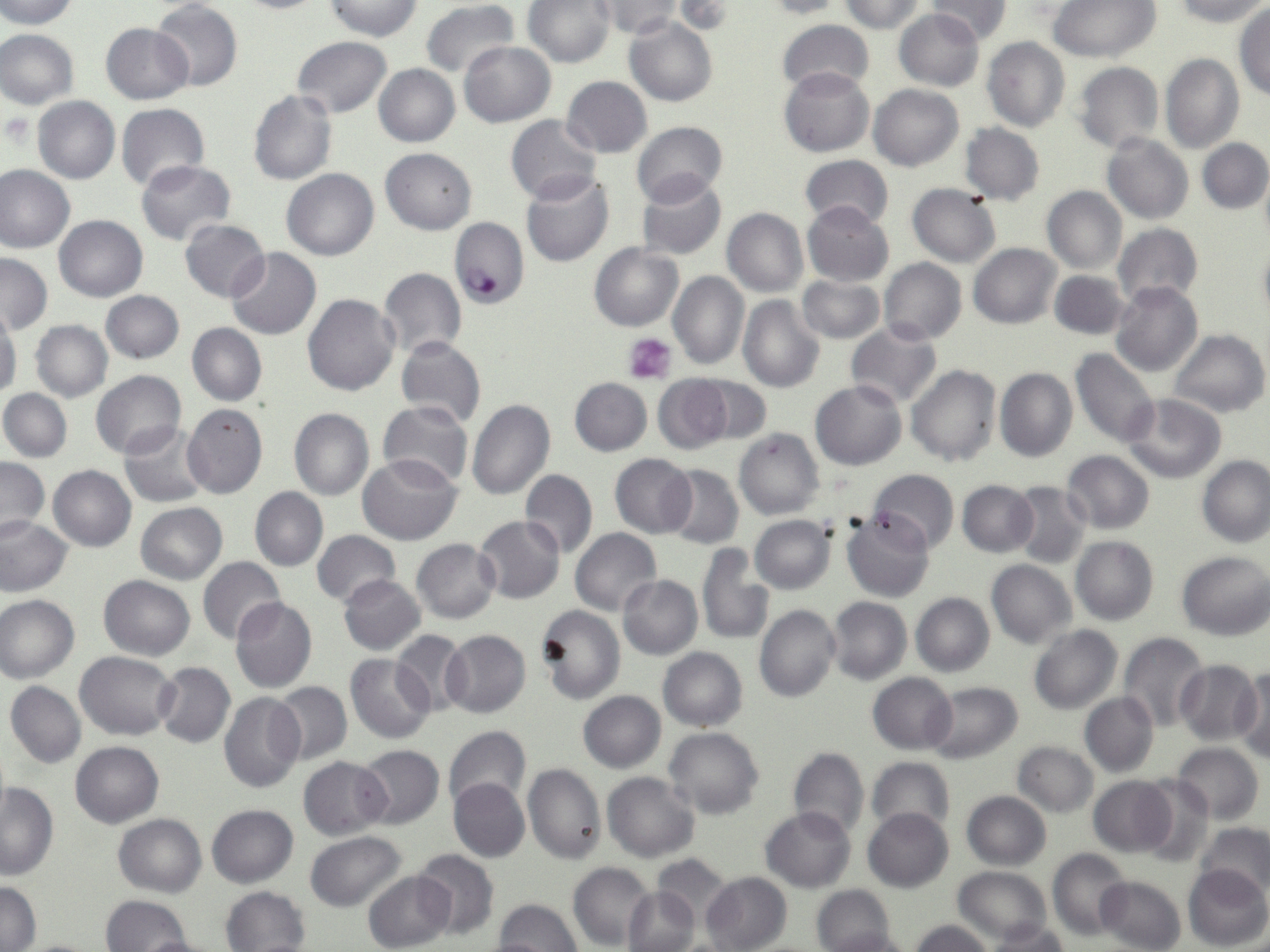

Summary:
  - Coordinate format: approximate bounding boxes as (x1,y1)-(x2,y2) corner pairs in pixels
  - Plasmodium falciparum-infected red blood cell locations: (449,217)-(528,309)
  - Uninfected red blood cell locations: (0,0)-(78,29), (227,0)-(332,13), (320,0)-(422,40), (421,0)-(520,80), (758,0)-(843,19), (836,0)-(929,32), (924,0)-(1010,43), (1049,0)-(1158,61), (1169,0)-(1270,26), (150,1)-(242,92), (523,1)-(615,69), (595,1)-(681,38), (675,1)-(736,35), (1233,4)-(1270,100), (894,8)-(984,91), (625,15)-(718,106), (777,20)-(874,98), (101,23)-(192,103), (0,28)-(79,108), (292,36)-(392,118), (982,38)-(1070,132), (458,41)-(556,126), (1160,53)-(1243,154), (1073,62)-(1164,154), (374,64)-(459,147), (779,67)-(874,157), (562,76)-(652,157), (869,84)-(964,170), (248,90)-(336,185), (33,96)-(121,184), (117,103)-(209,193), (505,114)-(603,203), (631,120)-(728,205), (960,123)-(1045,204), (1103,134)-(1193,224), (1198,139)-(1270,213), (380,147)-(476,234), (799,154)-(894,229), (136,159)-(237,245), (1258,164)-(1270,252), (0,165)-(75,254), (282,168)-(379,261), (521,173)-(613,267), (637,175)-(727,260), (906,183)-(1001,267), (1041,185)-(1127,274), (802,201)-(894,286), (722,207)-(808,295), (54,215)-(147,302), (180,219)-(270,302), (1112,223)-(1203,307), (1256,242)-(1270,324), (588,243)-(683,331), (969,243)-(1061,327), (225,248)-(322,339), (0,253)-(52,335), (879,258)-(966,344), (378,268)-(466,359), (1051,270)-(1129,340), (669,271)-(749,371), (797,276)-(885,344), (1110,281)-(1202,377), (101,291)-(183,364), (303,294)-(400,396), (738,295)-(826,393), (0,308)-(20,401), (30,320)-(112,402), (846,322)-(940,410), (188,323)-(266,406), (1167,329)-(1268,417), (397,336)-(486,428), (1070,348)-(1159,447), (907,365)-(1002,468), (995,368)-(1077,463), (90,371)-(186,459), (652,375)-(735,455), (686,375)-(773,446), (569,378)-(652,456), (810,380)-(907,470), (0,388)-(72,461), (1122,394)-(1227,484), (467,398)-(555,499), (378,400)-(474,489), (182,403)-(268,499), (288,408)-(373,500), (119,421)-(212,507), (734,429)-(824,519), (1062,450)-(1155,533), (610,453)-(697,537), (357,455)-(461,545), (0,456)-(49,541), (1197,456)-(1269,547), (49,465)-(136,552), (663,465)-(743,549), (520,469)-(597,557), (867,469)-(959,553), (957,481)-(1038,557), (1009,482)-(1091,568), (250,487)-(328,570), (136,502)-(227,584), (843,512)-(935,601), (473,514)-(565,604), (0,515)-(72,596), (749,515)-(835,594), (570,528)-(662,615), (311,530)-(400,607), (1071,536)-(1158,625), (411,539)-(499,623), (696,544)-(774,645), (1176,551)-(1270,640), (198,556)-(286,644), (986,560)-(1075,647), (339,574)-(425,655), (618,574)-(703,660), (98,575)-(194,660), (911,592)-(994,676), (1,595)-(79,683), (825,596)-(911,684), (229,597)-(317,693), (754,605)-(840,703), (536,606)-(625,704), (1029,625)-(1123,715), (441,629)-(530,718), (389,630)-(470,717), (1118,632)-(1209,733), (658,647)-(748,731), (76,651)-(177,739), (346,655)-(435,743), (1175,659)-(1262,746), (153,661)-(235,749), (1235,666)-(1270,760), (867,672)-(956,754), (5,681)-(86,768), (271,682)-(352,764), (925,682)-(1023,764), (578,690)-(667,771), (219,691)-(305,793), (1080,691)-(1159,777), (443,724)-(531,813), (663,727)-(764,819), (70,741)-(164,828), (1012,741)-(1099,816), (1172,743)-(1263,824), (356,745)-(444,830), (789,748)-(869,838), (298,755)-(390,840), (866,756)-(955,834), (523,764)-(606,864), (602,772)-(701,862), (1088,776)-(1177,856), (1136,777)-(1215,866), (448,778)-(529,862), (1,782)-(57,880), (960,791)-(1051,870), (206,804)-(298,887), (760,806)-(855,893), (863,808)-(954,892), (114,813)-(206,896), (1197,822)-(1270,897), (305,832)-(408,911), (1048,848)-(1133,941), (411,849)-(500,941), (651,854)-(734,925), (568,862)-(655,949), (1183,864)-(1270,950), (953,866)-(1051,942), (362,870)-(457,951), (702,872)-(792,952), (1096,876)-(1186,952), (1,879)-(40,950), (812,885)-(896,952), (221,886)-(310,952), (622,886)-(699,952), (102,894)-(192,952), (493,899)-(582,952), (910,919)-(995,952), (983,924)-(1073,952), (822,928)-(918,952), (130,935)-(223,952), (17,938)-(103,952)
  - Platelet locations: (4,114)-(36,147), (623,331)-(677,383)
  - Slide-level diagnosis: Plasmodium falciparum
  - Preparation: thin blood film
  - Field of view: single
  - Modality: light microscopy
  - Magnification: 1000x
  - Stain: May-Grünwald-Giemsa
  - Image size: 1270×952 pixels